Assess this cell for malaria.
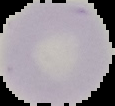

Uninfected.

{
  "preparation": "thin blood film",
  "image_type": "segmented cell region on a black background",
  "image_size": "115×106 pixels"
}